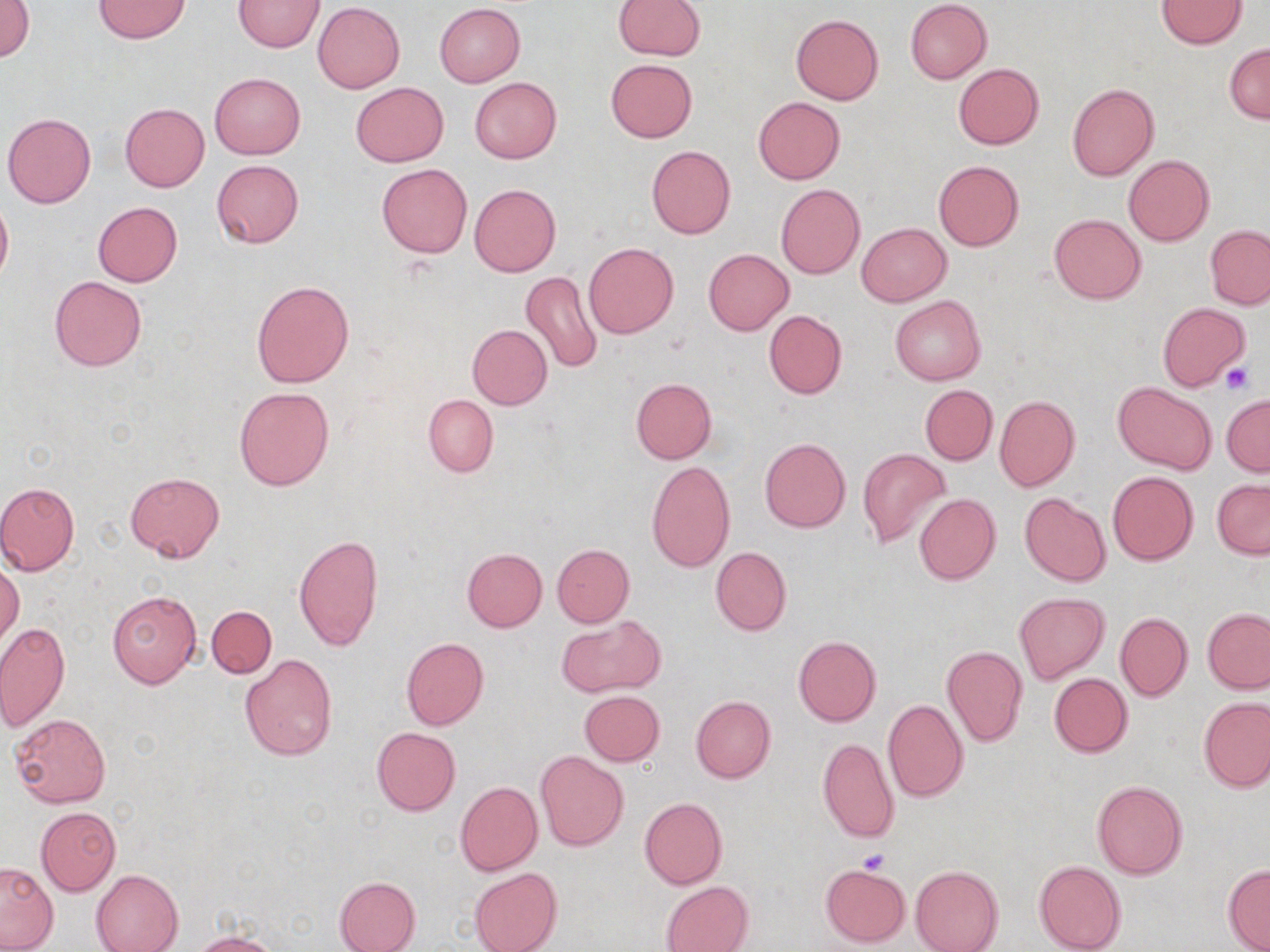 Approximate bounding boxes as named x1/y1/x2/y2 corners in pixels. Uninfected red blood cell locations: (x1=91, y1=0, x2=193, y2=43), (x1=233, y1=0, x2=324, y2=51), (x1=613, y1=0, x2=705, y2=59), (x1=0, y1=1, x2=34, y2=62), (x1=906, y1=1, x2=992, y2=84), (x1=1154, y1=1, x2=1249, y2=49), (x1=312, y1=2, x2=405, y2=94), (x1=435, y1=3, x2=525, y2=86), (x1=791, y1=14, x2=883, y2=104), (x1=1225, y1=43, x2=1269, y2=124), (x1=605, y1=58, x2=697, y2=142), (x1=953, y1=63, x2=1043, y2=150), (x1=210, y1=73, x2=305, y2=159), (x1=469, y1=77, x2=561, y2=163), (x1=351, y1=83, x2=449, y2=167), (x1=1068, y1=83, x2=1159, y2=181), (x1=752, y1=97, x2=844, y2=184), (x1=120, y1=103, x2=209, y2=191), (x1=2, y1=112, x2=96, y2=207), (x1=647, y1=145, x2=736, y2=240), (x1=1123, y1=154, x2=1215, y2=245), (x1=212, y1=159, x2=304, y2=247), (x1=933, y1=160, x2=1025, y2=252), (x1=376, y1=163, x2=472, y2=258), (x1=468, y1=183, x2=560, y2=276), (x1=775, y1=184, x2=865, y2=279), (x1=0, y1=192, x2=13, y2=285), (x1=93, y1=201, x2=183, y2=286), (x1=1051, y1=214, x2=1145, y2=304), (x1=856, y1=222, x2=951, y2=307), (x1=1205, y1=224, x2=1270, y2=309), (x1=583, y1=241, x2=679, y2=339), (x1=703, y1=248, x2=794, y2=335), (x1=521, y1=272, x2=602, y2=375), (x1=50, y1=276, x2=146, y2=372), (x1=251, y1=280, x2=354, y2=388), (x1=891, y1=296, x2=986, y2=385), (x1=1156, y1=302, x2=1251, y2=391), (x1=764, y1=309, x2=847, y2=398), (x1=467, y1=324, x2=552, y2=408), (x1=631, y1=377, x2=717, y2=463), (x1=1113, y1=383, x2=1216, y2=475), (x1=920, y1=384, x2=998, y2=465), (x1=233, y1=387, x2=335, y2=492), (x1=917, y1=391, x2=1070, y2=478), (x1=423, y1=395, x2=498, y2=477), (x1=994, y1=396, x2=1080, y2=493), (x1=1221, y1=396, x2=1269, y2=477), (x1=759, y1=438, x2=851, y2=533), (x1=858, y1=449, x2=951, y2=549), (x1=647, y1=461, x2=734, y2=571), (x1=1108, y1=471, x2=1198, y2=564), (x1=125, y1=472, x2=225, y2=563), (x1=1212, y1=478, x2=1270, y2=559), (x1=0, y1=481, x2=81, y2=575), (x1=1020, y1=493, x2=1110, y2=586), (x1=914, y1=494, x2=1001, y2=584), (x1=294, y1=534, x2=384, y2=652), (x1=551, y1=543, x2=634, y2=627), (x1=711, y1=547, x2=791, y2=636), (x1=462, y1=548, x2=547, y2=633), (x1=0, y1=561, x2=24, y2=647), (x1=107, y1=588, x2=203, y2=689), (x1=1015, y1=592, x2=1109, y2=683), (x1=207, y1=605, x2=277, y2=678), (x1=1203, y1=608, x2=1270, y2=693), (x1=1116, y1=612, x2=1193, y2=701), (x1=559, y1=614, x2=663, y2=697), (x1=0, y1=622, x2=70, y2=732), (x1=793, y1=636, x2=881, y2=727), (x1=401, y1=637, x2=488, y2=730), (x1=942, y1=646, x2=1027, y2=747), (x1=240, y1=654, x2=337, y2=761), (x1=1049, y1=672, x2=1133, y2=757), (x1=579, y1=690, x2=665, y2=766), (x1=691, y1=696, x2=776, y2=783), (x1=1200, y1=697, x2=1270, y2=792), (x1=882, y1=699, x2=969, y2=802), (x1=9, y1=713, x2=111, y2=807), (x1=371, y1=727, x2=461, y2=816), (x1=818, y1=736, x2=900, y2=845), (x1=536, y1=750, x2=628, y2=850), (x1=1091, y1=779, x2=1188, y2=879), (x1=455, y1=781, x2=542, y2=876), (x1=639, y1=797, x2=727, y2=889), (x1=36, y1=807, x2=121, y2=896), (x1=1033, y1=860, x2=1126, y2=952), (x1=0, y1=862, x2=59, y2=951), (x1=819, y1=863, x2=910, y2=948), (x1=1223, y1=864, x2=1270, y2=952), (x1=912, y1=865, x2=1003, y2=952), (x1=469, y1=867, x2=562, y2=952), (x1=91, y1=869, x2=184, y2=952), (x1=334, y1=876, x2=420, y2=952), (x1=662, y1=881, x2=753, y2=952), (x1=192, y1=933, x2=278, y2=952). Platelet locations: (x1=1221, y1=362, x2=1257, y2=395), (x1=856, y1=847, x2=892, y2=875). Slide-level diagnosis: negative for blood parasites. Image is 1270×952 pixels. Single field of view. Thin blood film. Optical microscopy. 1000x magnification. May-Grünwald-Giemsa-stained preparation.